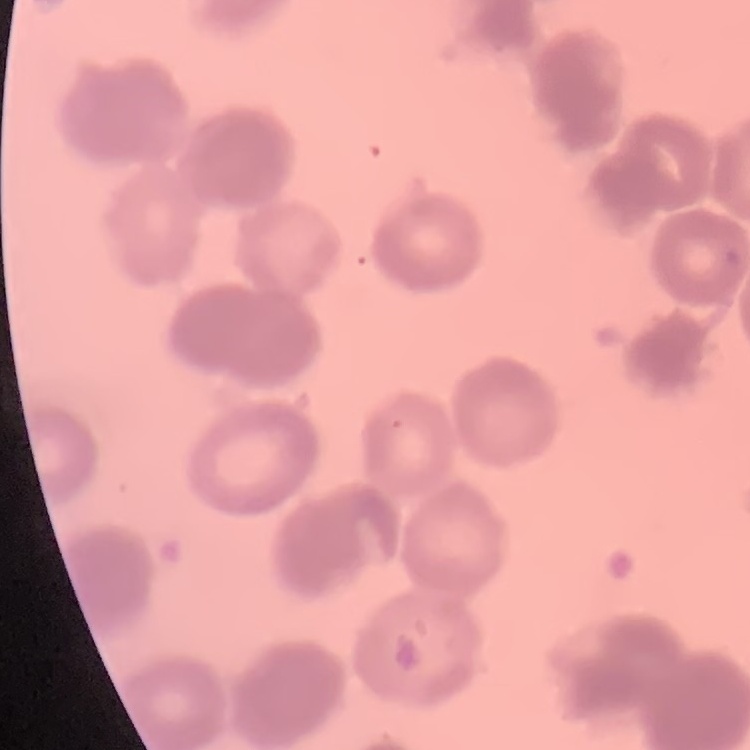
The erythrocytes show rouleaux formation. Field's or Giemsa stain. One tile cut from a larger photomicrograph. Thin peripheral smear.